Name the blood parasite species.
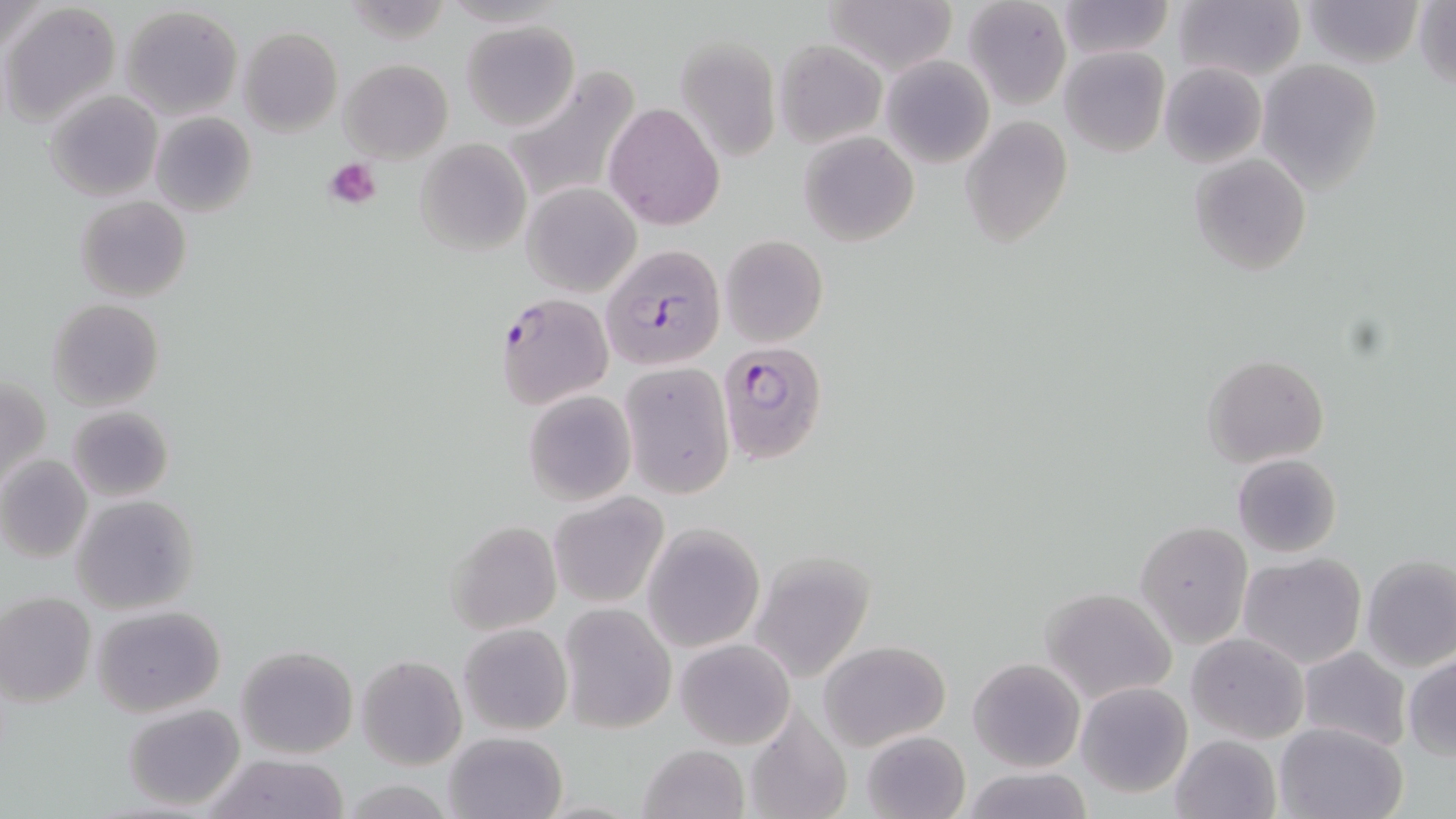

Plasmodium falciparum.

Approximate bounding boxes as [x1, y1, x2, y2] in pixels. Uninfected red blood cell locations: [824, 0, 958, 75], [963, 0, 1071, 111], [1055, 0, 1174, 59], [1173, 0, 1305, 83], [1301, 0, 1424, 68], [1414, 2, 1456, 92], [0, 3, 52, 59], [3, 3, 122, 127], [118, 5, 244, 119], [462, 19, 578, 130], [238, 26, 342, 136], [674, 35, 782, 162], [774, 40, 884, 145], [1059, 46, 1170, 158], [881, 56, 994, 168], [339, 58, 453, 163], [1257, 59, 1382, 191], [1159, 63, 1265, 168], [501, 65, 641, 212], [45, 91, 162, 202], [604, 102, 724, 230], [150, 111, 257, 217], [959, 114, 1074, 247], [798, 131, 919, 246], [415, 137, 532, 256], [1189, 152, 1312, 275], [521, 183, 640, 297], [75, 195, 190, 302], [721, 234, 827, 346], [47, 299, 164, 411], [1202, 353, 1331, 467], [619, 363, 735, 499], [1, 375, 50, 493], [522, 393, 635, 506], [68, 405, 174, 502], [1233, 453, 1342, 556], [0, 455, 93, 562], [547, 494, 668, 608], [71, 495, 199, 614], [445, 520, 562, 634], [1134, 520, 1252, 647], [643, 523, 764, 653], [749, 552, 876, 683], [1237, 553, 1368, 671], [1360, 556, 1456, 672], [1041, 587, 1179, 705], [0, 592, 97, 706], [558, 603, 678, 734], [91, 606, 225, 716], [459, 623, 572, 735], [1187, 632, 1308, 743], [675, 639, 794, 749], [818, 639, 950, 751], [236, 643, 359, 759], [1297, 646, 1413, 752], [1404, 653, 1456, 761], [357, 655, 465, 769], [967, 657, 1086, 772], [1075, 681, 1193, 798], [122, 703, 246, 813], [742, 708, 853, 819], [1273, 721, 1408, 819], [862, 730, 971, 819], [443, 731, 569, 819], [1170, 734, 1280, 819], [637, 745, 750, 819], [204, 753, 351, 818], [956, 766, 1098, 819]. Plasmodium falciparum-infected red blood cell locations: [600, 243, 726, 373], [495, 292, 613, 409], [717, 341, 828, 464]. Platelet locations: [325, 157, 383, 210]. Light microscopy. Image is 1456×819 pixels. Captured at 1000x magnification. May-Grünwald-Giemsa-stained preparation. Thin blood smear. Single field of view.